Assess this cell for malaria.
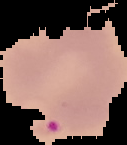
It is parasitized.

Summary:
  - Image type: segmented cell region with the area outside set to black
  - Image size: 127×145 pixels
  - Preparation: thin blood smear